Describe the morphology of the red blood cells.
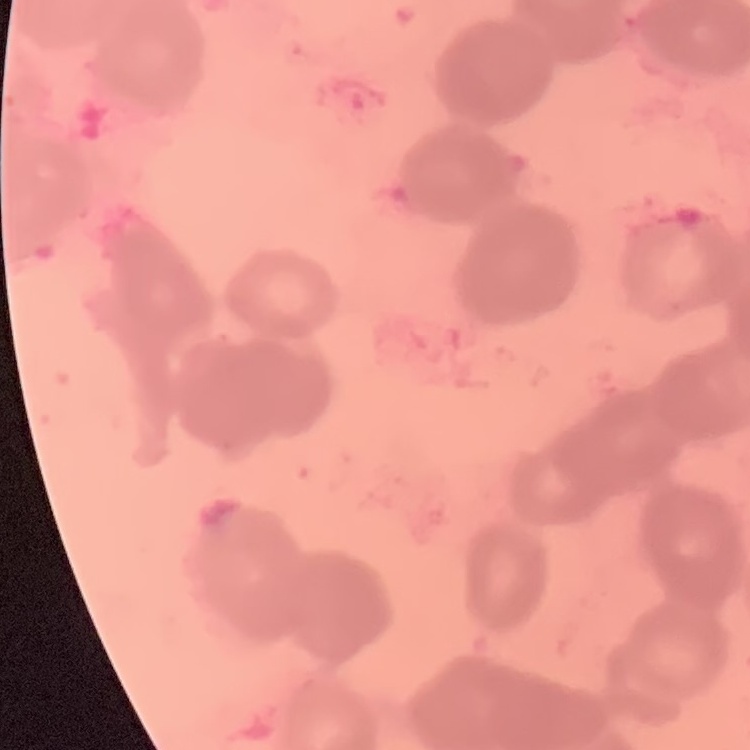
Rouleaux formation.

image type = one tile cut from a larger photomicrograph
preparation = thin blood smear
stain = Field's or Giemsa